Report the malaria status of this cell.
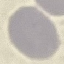
It is uninfected.

preparation = thin smear
stain = Giemsa
image type = cell patch, automatically extracted from a larger field of view and resized to 64 × 64 pixels
capture = smartphone through the microscope eyepiece